Classify this cell by malaria status.
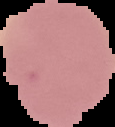
It is uninfected.

Summary:
  - Image type: cell region segmented out of the field of view; surrounding area masked to black
  - Preparation: thin blood smear
  - Image size: 115×127 pixels